Report the malaria status of this cell.
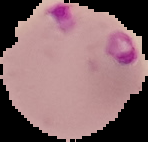
Parasitized.

Image is 148×142 pixels. Cell region segmented out of the field of view; the surrounding area is masked to black. From a thin blood film.